Describe the morphology of the red blood cells.
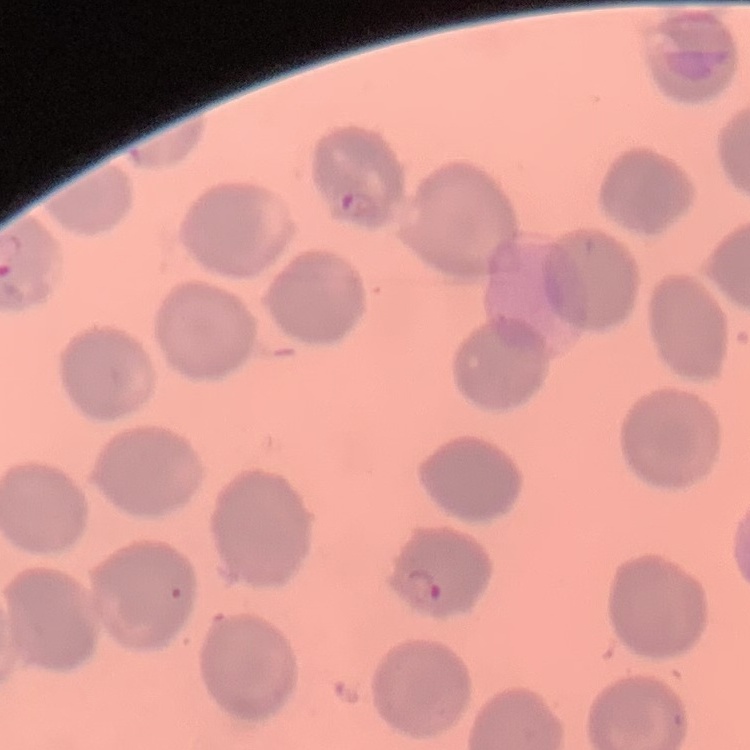
No rouleaux formation.

stain: Field's or Giemsa
image_type: one tile cut from a larger photomicrograph
preparation: thin blood film